Locate every blood parasite and identify its species.
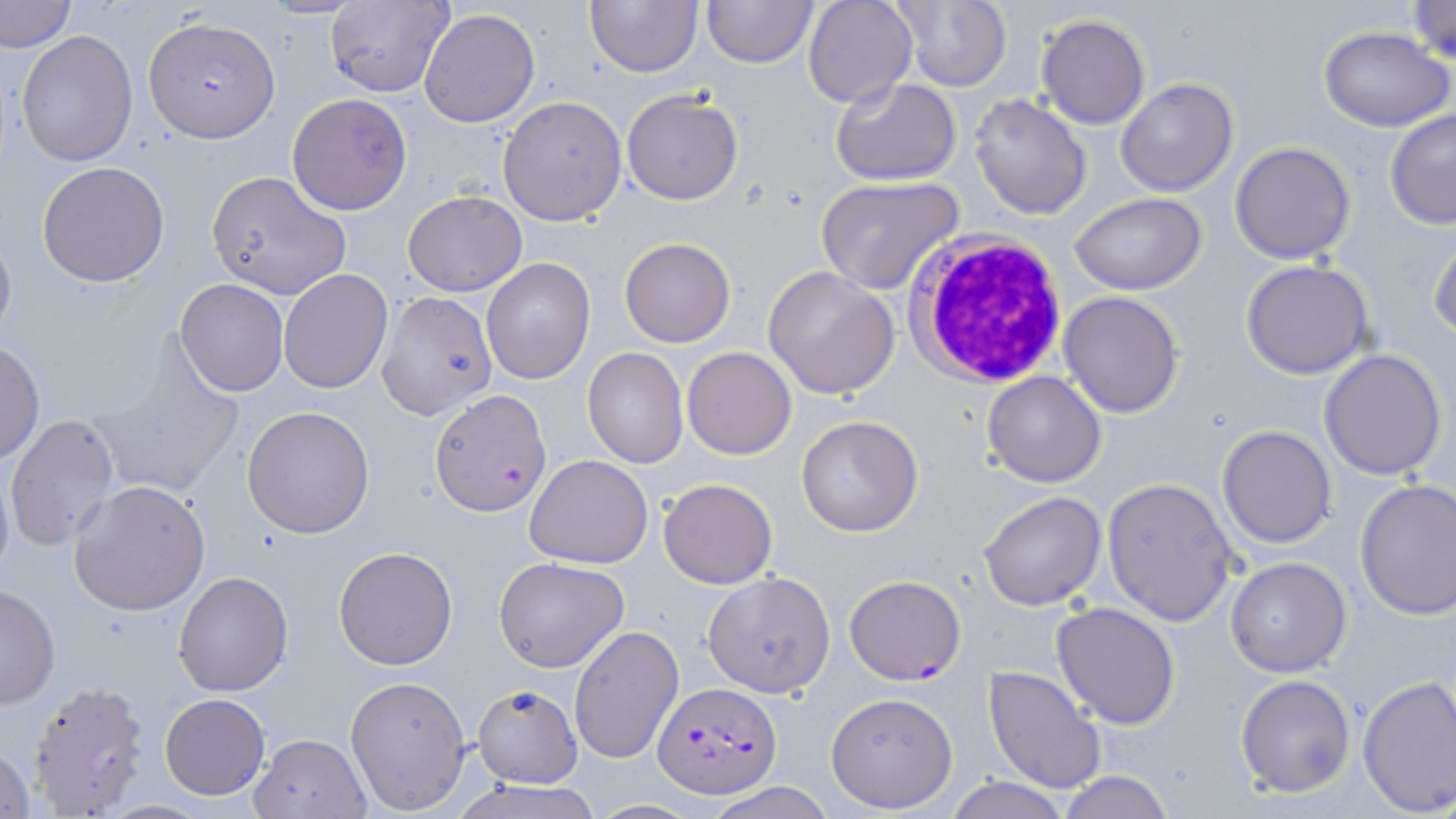
Approximate bounding boxes as named x1/y1/x2/y2 corners in pixels.
Plasmodium falciparum-infected red blood cells (subset): (x1=145, y1=15, x2=280, y2=140), (x1=432, y1=390, x2=550, y2=514), (x1=652, y1=683, x2=781, y2=798).
No Plasmodium ovale, Plasmodium malariae, Plasmodium vivax, Babesia divergens, or Trypanosoma brucei observed.

Summary:
  - Uninfected red blood cell locations (subset): (x1=1, y1=0, x2=75, y2=52), (x1=584, y1=0, x2=703, y2=77), (x1=701, y1=0, x2=818, y2=68), (x1=802, y1=0, x2=919, y2=109), (x1=891, y1=0, x2=1012, y2=90), (x1=1403, y1=0, x2=1455, y2=67), (x1=324, y1=1, x2=455, y2=98), (x1=418, y1=9, x2=540, y2=128), (x1=1036, y1=14, x2=1150, y2=130), (x1=1319, y1=26, x2=1455, y2=131), (x1=16, y1=31, x2=139, y2=167), (x1=831, y1=77, x2=961, y2=185), (x1=1115, y1=77, x2=1239, y2=197), (x1=622, y1=89, x2=744, y2=205), (x1=286, y1=93, x2=413, y2=215), (x1=968, y1=93, x2=1092, y2=220), (x1=497, y1=96, x2=627, y2=226), (x1=1384, y1=108, x2=1456, y2=229), (x1=1230, y1=141, x2=1357, y2=263), (x1=37, y1=161, x2=170, y2=286), (x1=205, y1=170, x2=351, y2=301), (x1=814, y1=177, x2=965, y2=294), (x1=403, y1=190, x2=528, y2=296), (x1=1069, y1=193, x2=1207, y2=293), (x1=0, y1=221, x2=16, y2=348), (x1=1428, y1=231, x2=1456, y2=342), (x1=619, y1=238, x2=736, y2=348), (x1=481, y1=258, x2=596, y2=385), (x1=1241, y1=261, x2=1373, y2=379), (x1=762, y1=266, x2=900, y2=400), (x1=278, y1=269, x2=392, y2=393), (x1=175, y1=279, x2=288, y2=396), (x1=375, y1=290, x2=497, y2=419), (x1=1059, y1=290, x2=1184, y2=417), (x1=0, y1=340, x2=44, y2=466), (x1=86, y1=345, x2=245, y2=499), (x1=682, y1=347, x2=796, y2=459), (x1=583, y1=348, x2=687, y2=467), (x1=1318, y1=348, x2=1449, y2=479), (x1=983, y1=371, x2=1107, y2=488), (x1=242, y1=405, x2=376, y2=539), (x1=6, y1=413, x2=120, y2=552), (x1=797, y1=416, x2=922, y2=537), (x1=1216, y1=424, x2=1338, y2=549), (x1=524, y1=455, x2=653, y2=568), (x1=0, y1=459, x2=14, y2=591), (x1=1102, y1=477, x2=1238, y2=626), (x1=658, y1=478, x2=777, y2=589), (x1=67, y1=479, x2=211, y2=617), (x1=1355, y1=479, x2=1456, y2=620), (x1=978, y1=491, x2=1106, y2=611), (x1=333, y1=545, x2=458, y2=669), (x1=1226, y1=557, x2=1350, y2=677), (x1=495, y1=558, x2=628, y2=673), (x1=173, y1=570, x2=293, y2=696), (x1=702, y1=570, x2=836, y2=697), (x1=0, y1=582, x2=59, y2=709), (x1=1051, y1=602, x2=1181, y2=728), (x1=569, y1=624, x2=684, y2=764), (x1=983, y1=666, x2=1107, y2=794), (x1=1356, y1=673, x2=1456, y2=817), (x1=344, y1=675, x2=471, y2=814), (x1=1235, y1=675, x2=1356, y2=797), (x1=27, y1=680, x2=151, y2=816), (x1=825, y1=691, x2=959, y2=812), (x1=475, y1=692, x2=583, y2=790), (x1=160, y1=694, x2=270, y2=800), (x1=249, y1=731, x2=371, y2=818), (x1=0, y1=745, x2=35, y2=819), (x1=1056, y1=772, x2=1178, y2=819), (x1=945, y1=775, x2=1069, y2=818), (x1=451, y1=778, x2=605, y2=819), (x1=704, y1=783, x2=837, y2=819)
  - White blood cell locations: (x1=908, y1=231, x2=1070, y2=386)
  - Slide-level diagnosis: Plasmodium falciparum
  - Field of view: single
  - Stain: May-Grünwald-Giemsa
  - Image size: 1456×819 pixels
  - Preparation: thin blood smear
  - Magnification: 1000x
  - Modality: light microscopy